Assess this cell for malaria.
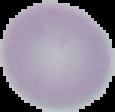
Uninfected.

Summary:
  - Image size: 115×112 pixels
  - Preparation: thin blood smear
  - Image type: cell region segmented out of the field of view; surrounding area masked to black